State which cell type is depicted.
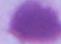

This is an erythrocyte.

{
  "magnification": "1000x",
  "modality": "photomicrograph"
}